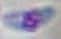

1000x magnification. Photomicrograph. Toxoplasma gondii is shown.